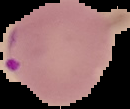
Summary:
  - Image type: segmented cell region with the area outside set to black
  - Image size: 130×109 pixels
  - Result: Plasmodium parasites identified
  - Preparation: thin blood film